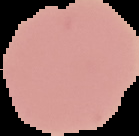
Image is 139×136 pixels. Malaria status: uninfected. From a thin blood film. Cell region segmented out of the field of view; the surrounding area is masked to black.